Assess for Plasmodium parasites.
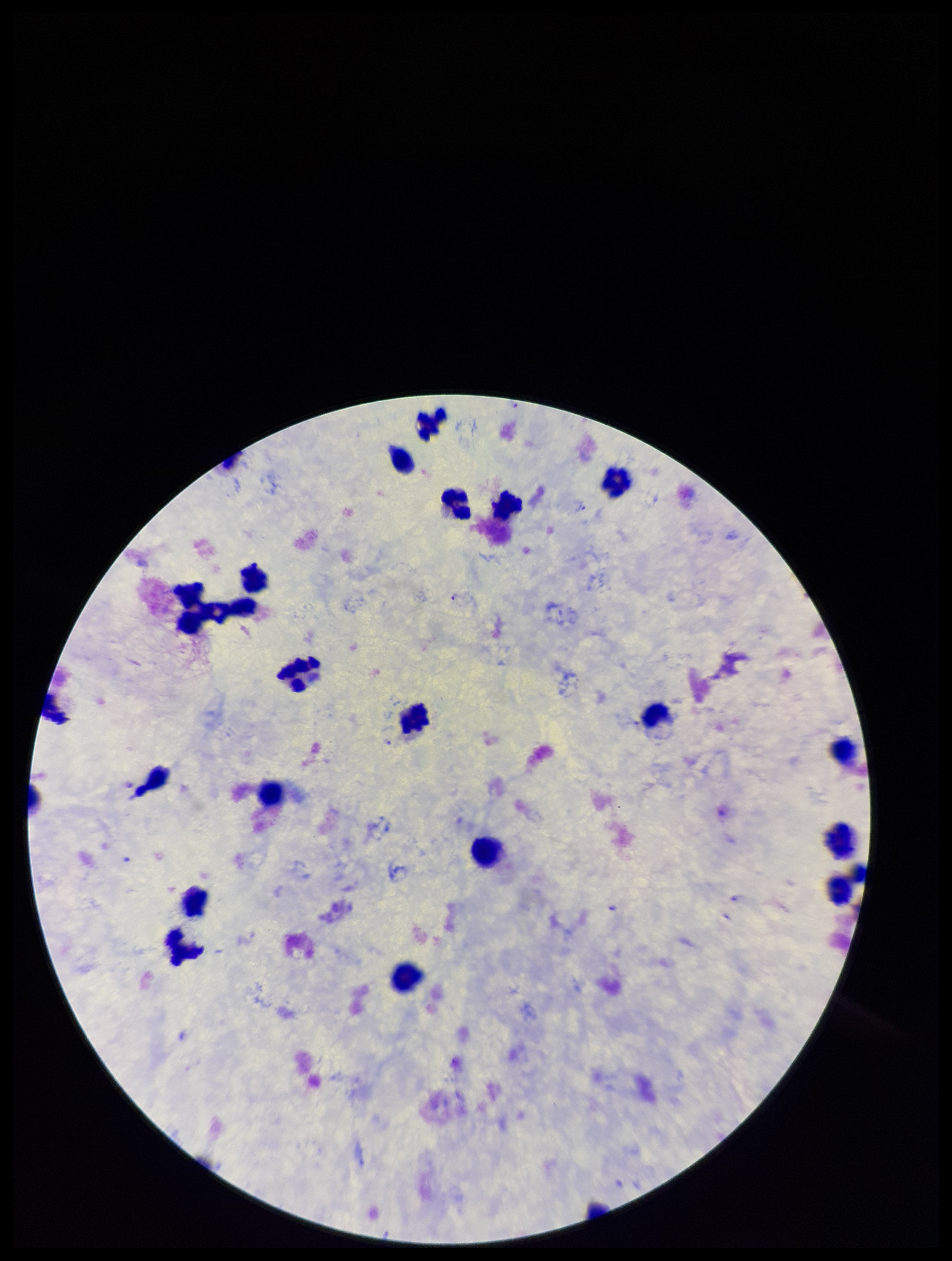
Detected.

Summary:
  - Stain: Giemsa
  - Field of view: single
  - Capture: smartphone photograph through the microscope eyepiece
  - Preparation: thick
  - Leukocyte count: 21
  - Image size: 952×1261 pixels
  - Parasite count: 2
  - Patient malaria status: positive
  - Species reported for this patient: Plasmodium falciparum